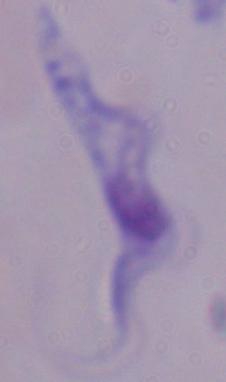

Summary:
  - Identification: trypanosome
  - Magnification: 1000x
  - Modality: micrograph